Report the malaria status of this cell.
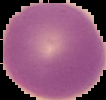
Uninfected.

Cell region segmented out of the field of view; the surrounding area is masked to black. Image is 106×100 pixels. From a thin blood smear.